Classify this cell by malaria status.
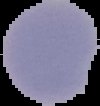

It is parasitized.

image size = 100×106 pixels
image type = segmented cell region with the area outside set to black
preparation = thin blood smear